Report the malaria status of this cell.
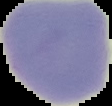
Uninfected.

Summary:
  - Preparation: thin blood smear
  - Image type: segmented cell region with the area outside set to black
  - Image size: 112×106 pixels